Describe the morphology of the red blood cells.
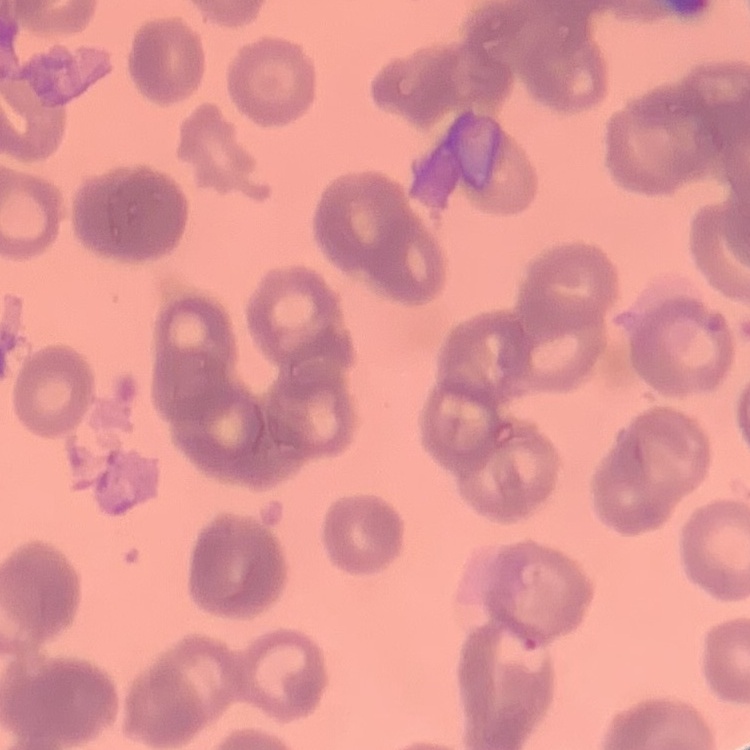
They show rouleaux formation.

Summary:
  - Image type: square crop of a larger photomicrograph
  - Stain: Field's or Giemsa
  - Preparation: thin blood film